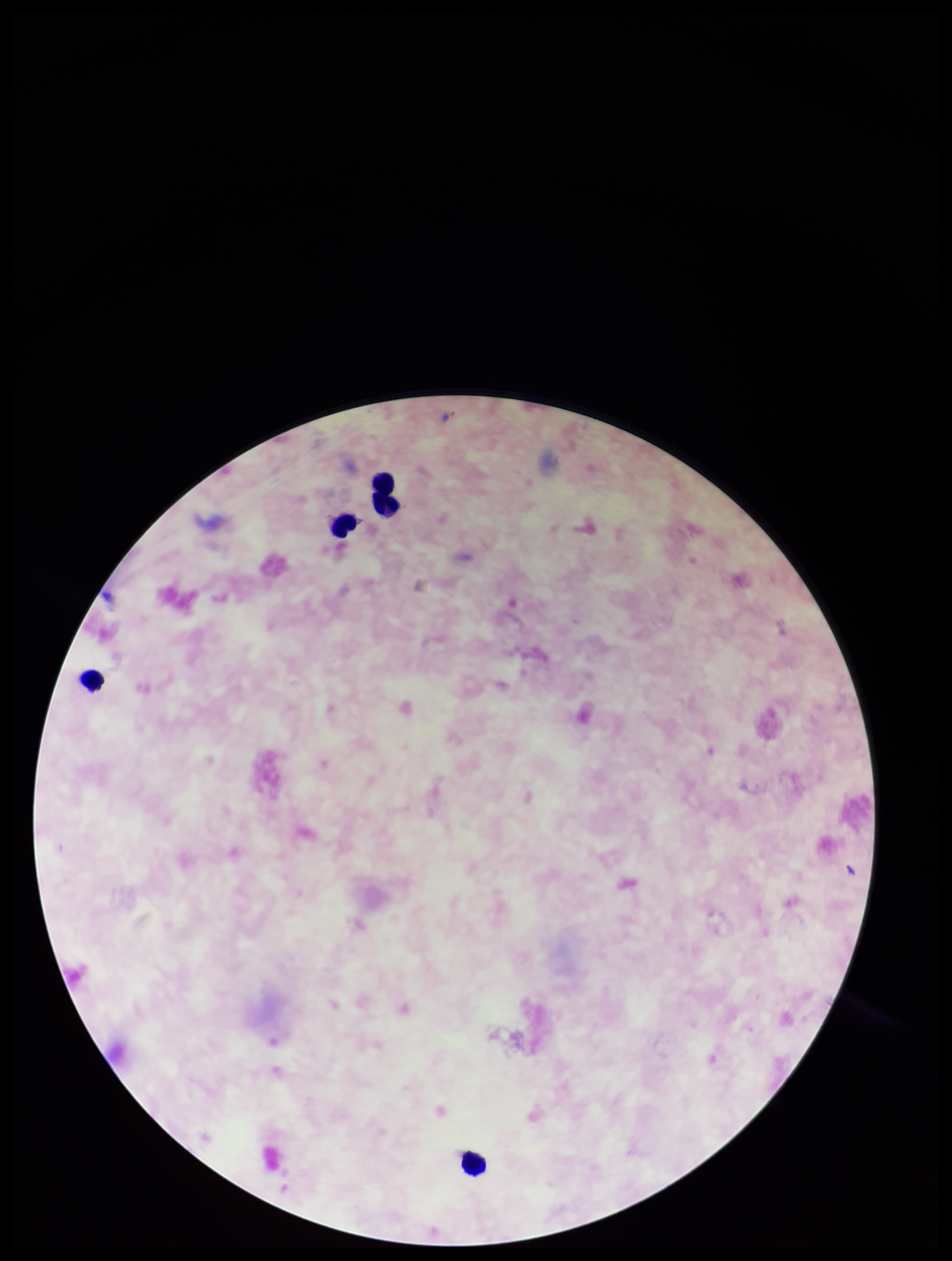
{
  "field_of_view": "single",
  "capture": "smartphone photograph through the microscope eyepiece",
  "stain": "Giemsa",
  "plasmodium_parasites": "none seen",
  "image_size": "952×1261 pixels",
  "parasite_count": 0,
  "preparation": "thick blood smear",
  "patient_malaria_status": "negative",
  "leukocyte_count": 5
}